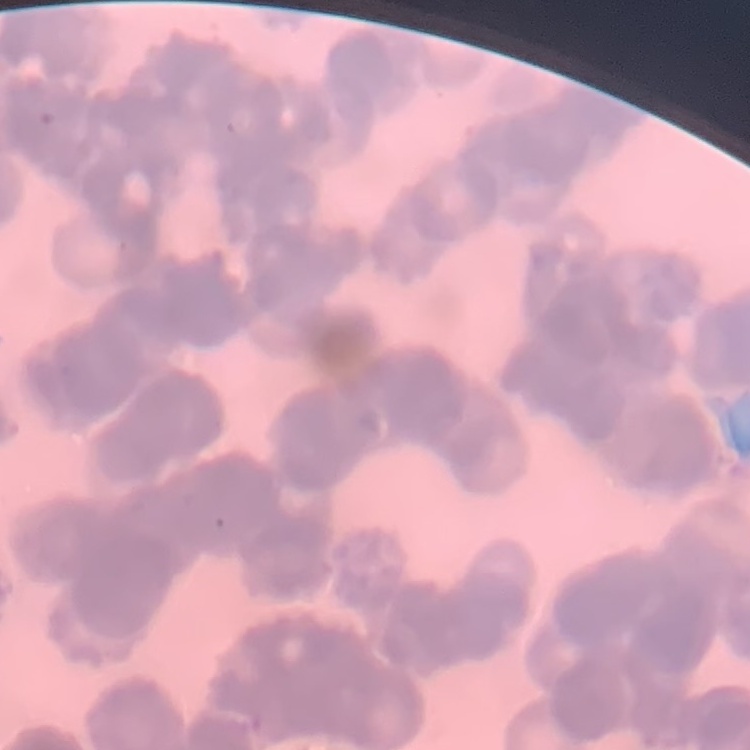

Summary:
  - Red blood cell morphology: rouleaux formation
  - Image type: one tile cut from a larger photomicrograph
  - Preparation: thin peripheral smear
  - Stain: Field's or Giemsa